Locate every Plasmodium vivax-infected red blood cell.
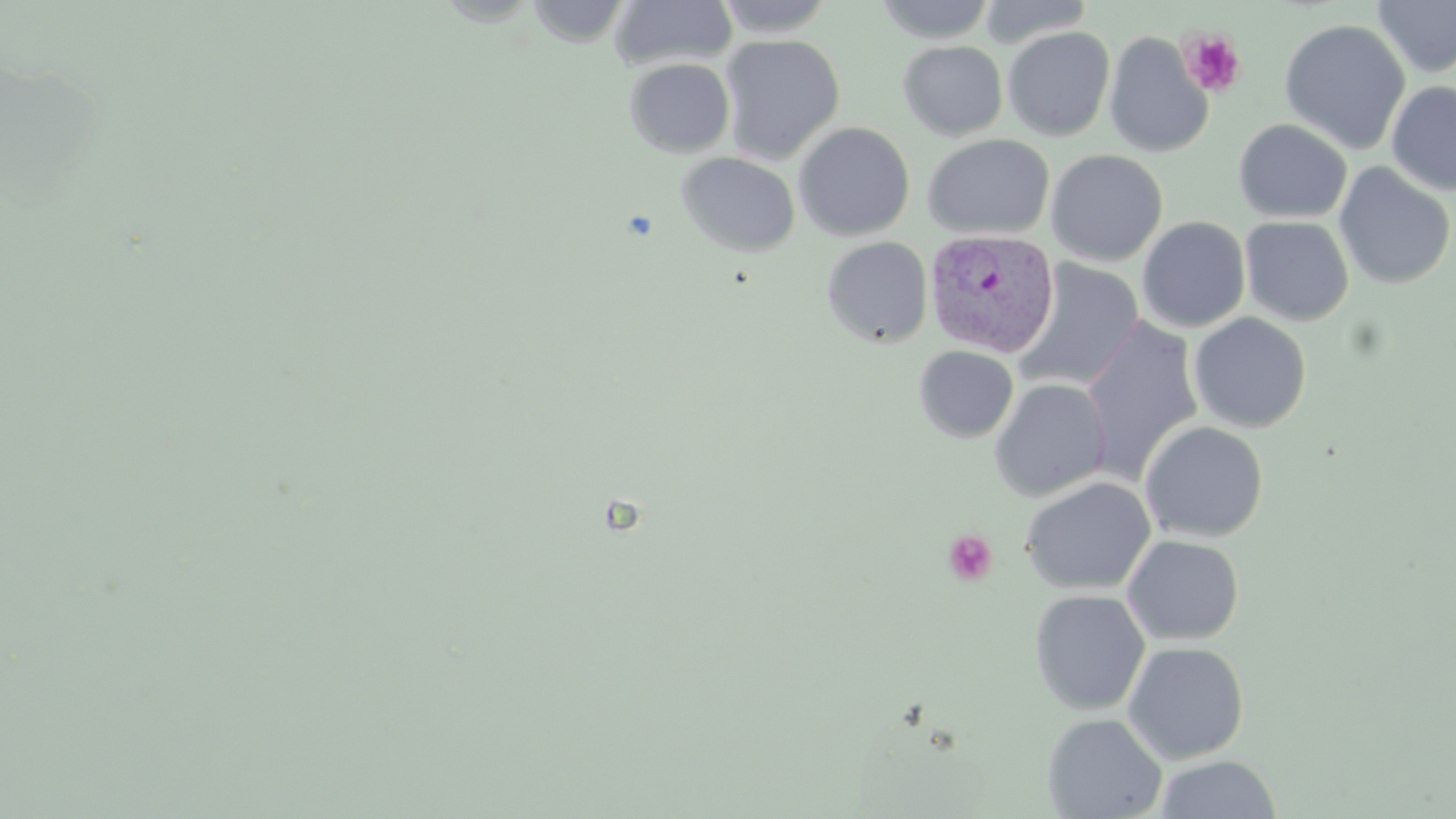
Approximate bounding boxes as (x1,y1)-(x2,y2) corner pairs in pixels.
Plasmodium vivax-infected red blood cells: (925,229)-(1059,358).

Uninfected red blood cell locations: (610,0)-(738,71), (714,0)-(837,37), (975,0)-(1095,49), (1372,0)-(1456,78), (527,1)-(633,47), (874,1)-(996,43), (1279,18)-(1411,155), (1003,26)-(1115,141), (1103,32)-(1214,158), (719,34)-(846,164), (897,41)-(1008,141), (624,58)-(736,158), (1386,80)-(1456,196), (1233,119)-(1352,223), (793,121)-(915,241), (922,133)-(1055,239), (1046,149)-(1168,266), (675,151)-(801,257), (1334,162)-(1455,289), (1137,216)-(1251,332), (1239,216)-(1354,326), (822,236)-(932,348), (1014,258)-(1144,392), (1188,312)-(1312,433), (1082,317)-(1203,482), (914,345)-(1019,443), (989,378)-(1111,501), (1139,421)-(1269,542), (1020,476)-(1156,595), (1122,534)-(1245,645), (1029,589)-(1150,716), (1122,641)-(1249,763), (1042,712)-(1167,819), (1154,754)-(1283,818). Platelet locations: (1177,29)-(1247,98), (943,530)-(998,586). Slide-level diagnosis: Plasmodium vivax. 1000x magnification. Optical microscopy. Image is 1456×819 pixels. One field of a larger specimen. Thin blood smear. May-Grünwald-Giemsa-stained preparation.